State the blood parasite species.
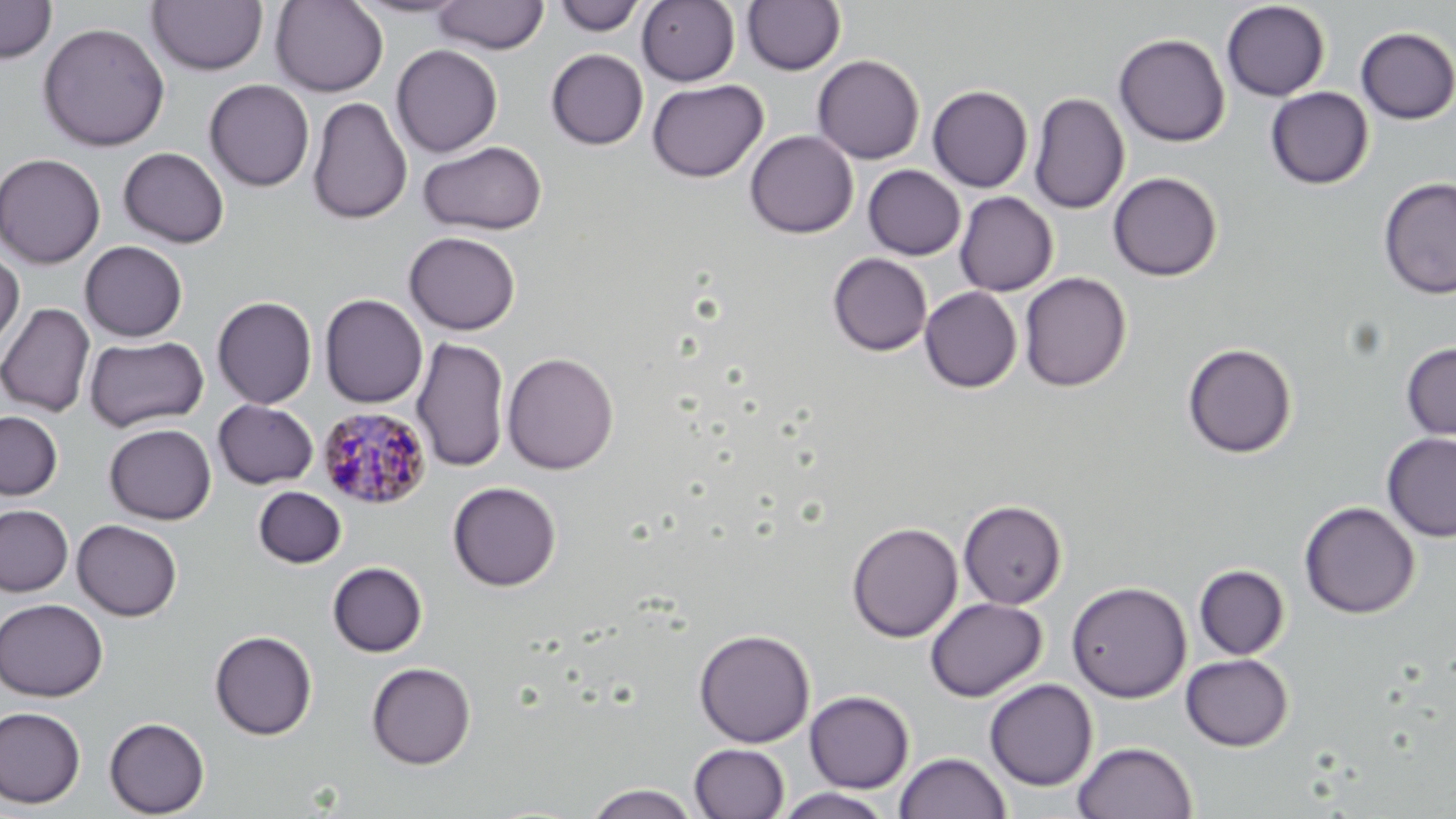
Plasmodium malariae.

Approximate bounding boxes as (x1,y1)-(x2,y2) corner pairs in pixels. Plasmodium malariae-infected red blood cell locations: (316,405)-(433,511). Uninfected red blood cell locations: (0,0)-(57,63), (146,0)-(268,76), (346,0)-(472,19), (431,0)-(550,54), (637,0)-(740,86), (741,0)-(845,75), (270,1)-(389,96), (553,1)-(647,35), (1221,1)-(1330,101), (37,21)-(171,151), (1356,26)-(1456,124), (1114,33)-(1230,147), (391,44)-(503,157), (545,48)-(649,149), (812,55)-(925,164), (204,79)-(315,191), (647,79)-(768,183), (927,85)-(1033,192), (1265,86)-(1374,190), (1029,92)-(1130,215), (307,96)-(412,225), (744,130)-(858,239), (418,141)-(547,235), (118,147)-(230,248), (0,152)-(106,269), (863,165)-(966,260), (1107,172)-(1222,280), (1377,177)-(1456,299), (955,192)-(1058,296), (403,231)-(521,335), (79,240)-(188,342), (0,246)-(25,354), (827,253)-(932,356), (1019,272)-(1131,392), (920,286)-(1022,393), (319,294)-(428,408), (212,296)-(317,409), (0,302)-(96,417), (84,335)-(209,432), (412,336)-(511,473), (1401,341)-(1456,441), (1182,342)-(1297,457), (502,352)-(619,475), (213,400)-(319,489), (0,410)-(63,501), (104,423)-(216,524), (1381,433)-(1456,542), (447,481)-(562,591), (253,486)-(346,568), (945,500)-(1056,703), (958,500)-(1067,609), (1299,501)-(1420,619), (0,504)-(74,596), (71,519)-(182,621), (846,521)-(963,642), (327,561)-(428,657), (1194,565)-(1290,660), (1066,580)-(1192,703), (925,597)-(1047,702), (0,598)-(108,701), (694,628)-(815,747), (209,630)-(318,740), (1180,653)-(1293,751), (366,662)-(476,769), (984,678)-(1098,791), (804,690)-(914,793), (0,707)-(86,808), (104,716)-(210,818), (1072,741)-(1197,819), (689,743)-(789,819), (894,752)-(1010,819), (584,783)-(702,818), (773,788)-(894,819). One field of a larger specimen. Thin blood smear. Image is 1456×819 pixels. Captured at 1000x magnification. May-Grünwald-Giemsa-stained preparation. Light microscopy.